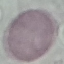

Summary:
  - Result: no malaria parasites seen
  - Preparation: thin blood film
  - Capture: smartphone camera at the microscope eyepiece
  - Image type: automatically extracted cell patch, resized to 64 × 64 pixels
  - Stain: Giemsa